Locate every blood parasite and identify its species.
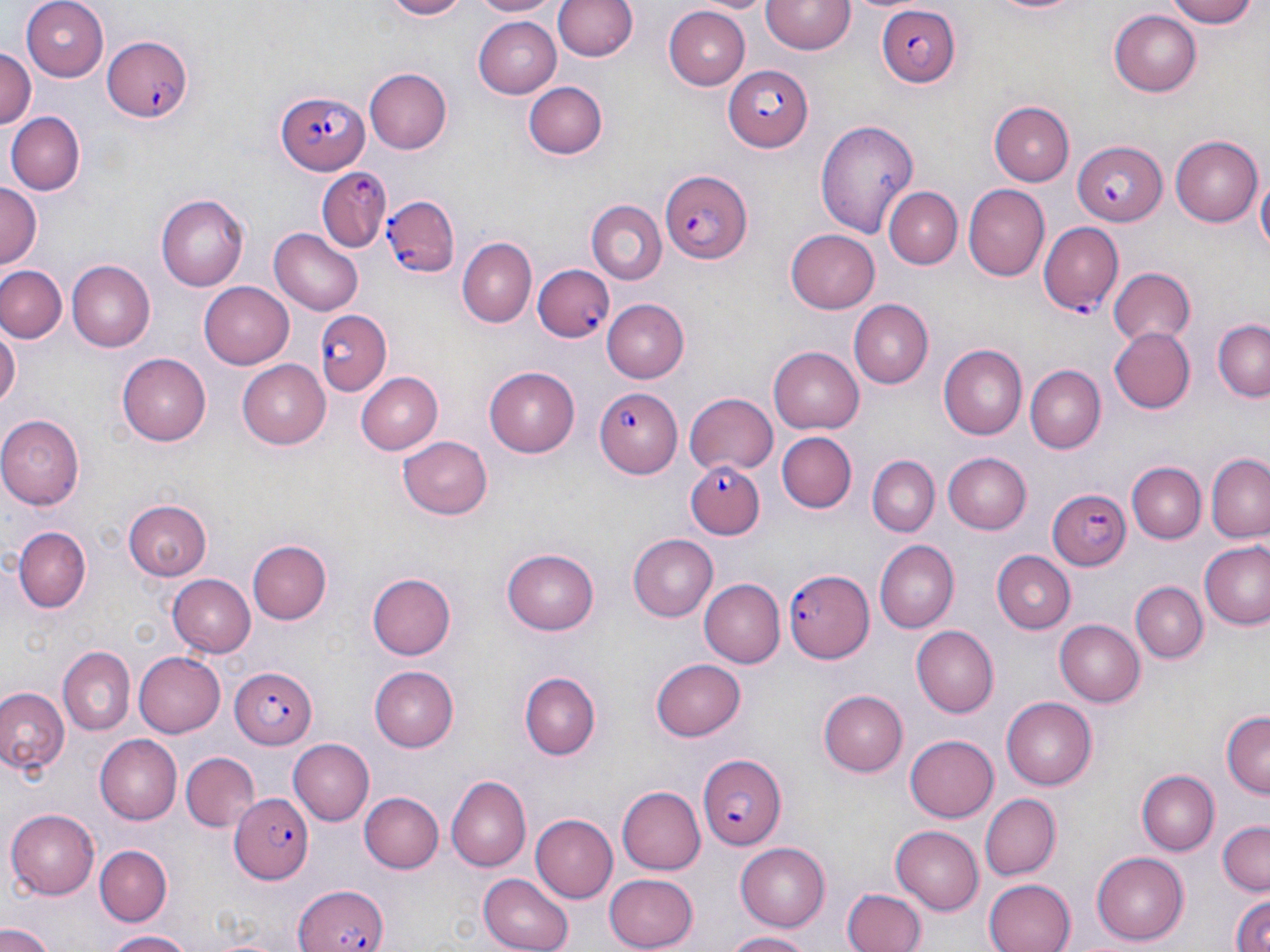

Approximate bounding boxes as (x1,y1)-(x2,y2) corner pairs in pixels.
Plasmodium falciparum-infected red blood cells: (874,6)-(959,87), (102,32)-(195,124), (723,64)-(815,151), (276,89)-(369,175), (1072,139)-(1169,225), (316,167)-(390,253), (659,168)-(752,265), (381,192)-(461,275), (1037,221)-(1124,316), (533,264)-(614,344), (316,313)-(393,396), (595,387)-(682,480), (688,458)-(766,541), (1047,488)-(1130,572), (784,568)-(873,662), (229,667)-(318,748), (697,750)-(785,850), (232,792)-(315,883), (295,882)-(388,952).
No Plasmodium ovale, Plasmodium malariae, Plasmodium vivax, Babesia divergens, or Trypanosoma brucei observed.

slide_level_diagnosis: Plasmodium falciparum
preparation: thin blood film
magnification: 1000x
stain: May-Grünwald-Giemsa
field_of_view: single
image_size: 1270×952 pixels
uninfected_red_blood_cell_locations: 'approximate bounding boxes as (x1,y1)-(x2,y2) corner pairs in pixels: (24,0)-(109,82), (372,0)-(474,20), (470,0)-(561,18), (553,0)-(638,64), (698,0)-(775,14), (763,0)-(855,55), (982,0)-(1094,17), (1170,0)-(1260,27), (663,7)-(749,88), (1110,8)-(1202,96), (471,16)-(560,97), (0,47)-(36,135), (363,68)-(451,155), (524,81)-(608,161), (989,101)-(1074,185), (5,112)-(82,196), (815,120)-(918,238), (1169,136)-(1260,226), (1256,173)-(1269,264), (0,183)-(42,270), (963,184)-(1050,281), (886,187)-(962,268), (157,195)-(249,292), (585,202)-(666,286), (270,227)-(366,314), (786,228)-(881,312), (457,238)-(537,327), (65,260)-(153,354), (1,265)-(66,343), (1107,268)-(1195,348), (198,281)-(294,368), (601,298)-(688,382), (849,299)-(932,386), (1212,320)-(1270,402), (0,322)-(19,414), (1108,326)-(1194,413), (939,344)-(1030,439), (769,347)-(864,434), (118,354)-(210,444), (237,359)-(334,449), (485,366)-(581,453), (1027,366)-(1104,451), (358,371)-(443,454), (684,392)-(777,475), (0,415)-(82,508), (775,430)-(857,512), (396,436)-(495,522), (944,452)-(1032,534), (1208,455)-(1270,543), (866,457)-(938,538), (1126,463)-(1206,544), (122,500)-(210,580), (13,525)-(92,611), (628,534)-(718,621), (247,540)-(333,624), (874,540)-(957,633), (1201,541)-(1270,629), (503,547)-(599,634), (993,552)-(1075,634), (367,573)-(457,659), (168,574)-(256,657), (699,579)-(784,668), (1130,582)-(1206,662), (1056,619)-(1145,707), (913,627)-(998,716), (61,647)-(136,735), (134,651)-(226,737), (653,658)-(745,741), (372,666)-(461,751), (519,670)-(604,760), (0,686)-(68,777), (819,691)-(907,776), (1002,697)-(1098,788), (1221,712)-(1269,798), (93,735)-(180,823), (906,735)-(999,821), (288,739)-(372,824), (181,750)-(259,832), (1138,770)-(1218,854), (445,777)-(529,871), (617,786)-(705,874), (360,792)-(443,873), (979,793)-(1061,879), (542,798)-(704,882), (7,808)-(101,897), (532,814)-(617,901), (1218,819)-(1269,894), (891,827)-(983,913), (735,842)-(831,931), (95,844)-(172,924), (1091,852)-(1189,944), (602,871)-(698,950), (478,873)-(572,952), (983,877)-(1077,952), (842,889)-(924,952), (1227,891)-(1270,952), (0,922)-(56,952), (103,930)-(198,951), (724,930)-(817,950)'
modality: light microscopy